Assess the morphology of the erythrocytes.
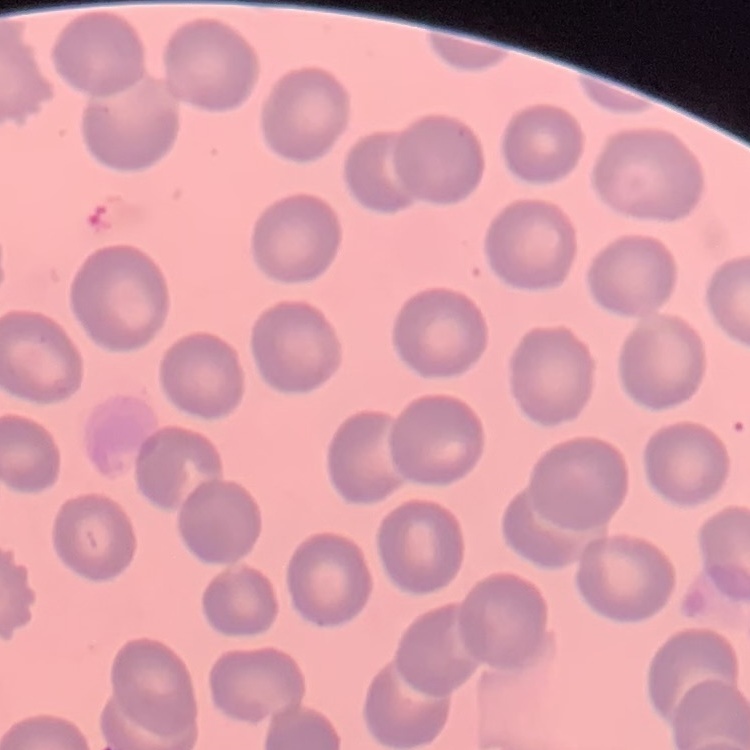

No rouleaux formation.

image type = square crop of a larger photomicrograph
stain = Field's or Giemsa
preparation = thin blood film